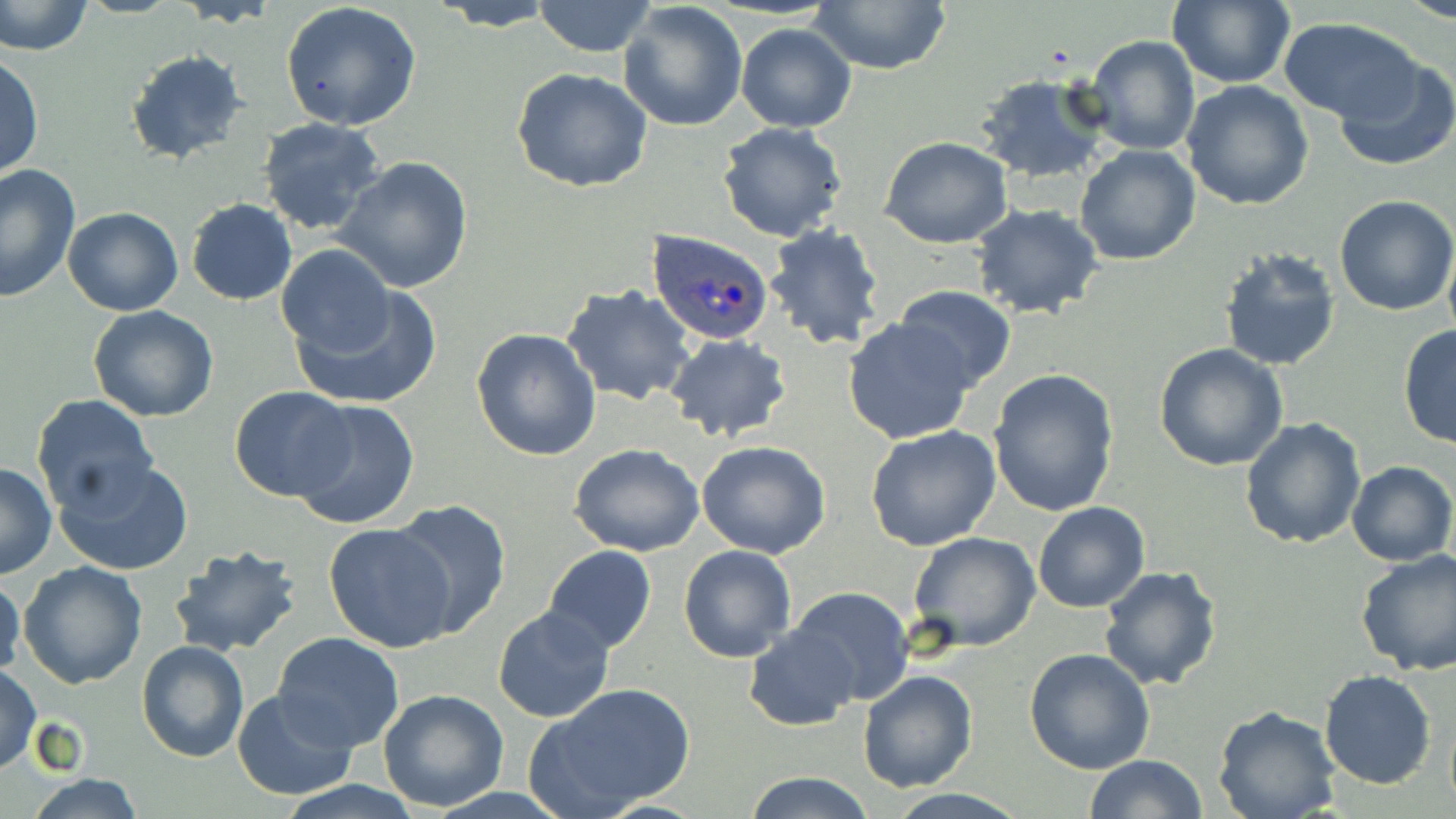
Summary:
  - Coordinate format: approximate bounding boxes as (x1,y1)-(x2,y2) corner pairs in pixels
  - Plasmodium ovale-infected red blood cell locations: (648,229)-(774,344)
  - Uninfected red blood cell locations: (0,0)-(94,56), (532,0)-(655,57), (1167,0)-(1294,88), (430,1)-(561,31), (808,1)-(952,77), (619,2)-(748,134), (280,3)-(423,132), (1279,17)-(1427,126), (735,22)-(857,133), (1083,35)-(1200,155), (1,50)-(43,181), (124,50)-(253,168), (1331,59)-(1456,170), (512,68)-(655,193), (975,70)-(1112,186), (1181,81)-(1315,211), (256,118)-(387,237), (718,121)-(849,243), (880,136)-(1013,249), (1074,144)-(1201,265), (333,156)-(473,295), (0,163)-(80,303), (1333,193)-(1456,316), (186,198)-(296,305), (970,202)-(1104,320), (61,207)-(183,315), (763,224)-(890,351), (277,245)-(394,357), (1443,245)-(1456,345), (1219,247)-(1342,371), (290,284)-(443,411), (561,285)-(695,406), (894,286)-(1017,391), (88,305)-(220,422), (842,317)-(977,445), (1398,324)-(1455,450), (471,329)-(601,462), (665,334)-(792,442), (1153,343)-(1289,471), (987,369)-(1120,518), (228,386)-(352,501), (31,396)-(160,516), (291,398)-(420,530), (1240,417)-(1366,550), (864,425)-(1003,551), (696,439)-(831,559), (570,442)-(705,557), (56,457)-(193,576), (1345,461)-(1456,566), (0,462)-(56,579), (391,499)-(510,637), (1032,501)-(1151,614), (322,521)-(456,652), (908,531)-(1041,653), (543,544)-(656,653), (678,544)-(797,664), (168,545)-(303,657), (1354,549)-(1456,676), (17,560)-(148,688), (1097,564)-(1222,691), (0,571)-(25,684), (786,584)-(914,710), (493,606)-(616,724), (743,624)-(860,731), (273,633)-(404,750), (135,640)-(250,763), (1023,648)-(1155,773), (0,666)-(43,774), (858,669)-(979,792), (1320,670)-(1436,790), (531,683)-(696,814), (231,690)-(361,801), (378,690)-(509,811), (1212,706)-(1342,819), (1085,754)-(1207,819), (746,772)-(875,819), (20,774)-(151,819), (274,782)-(426,818), (882,790)-(1028,819)
  - Slide-level diagnosis: Plasmodium ovale
  - Field of view: single
  - Stain: May-Grünwald-Giemsa
  - Modality: light microscopy
  - Magnification: 1000x
  - Preparation: thin blood smear
  - Image size: 1456×819 pixels